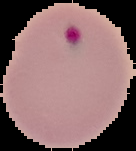

preparation = thin blood film
result = Plasmodium parasites identified
image type = cell region segmented out of the field of view; surrounding area masked to black
image size = 136×151 pixels